Name the parasite shown.
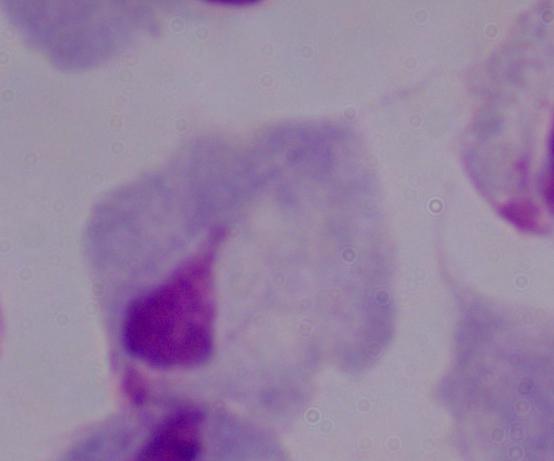
This is a trichomonad.

modality = photomicrograph
magnification = 1000x